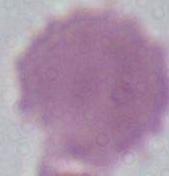

Summary:
  - Modality: photomicrograph
  - Magnification: 1000x
  - Identification: erythrocyte